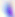 Micrograph. Toxoplasma gondii is seen. Captured at 400x magnification.